State the preparation type.
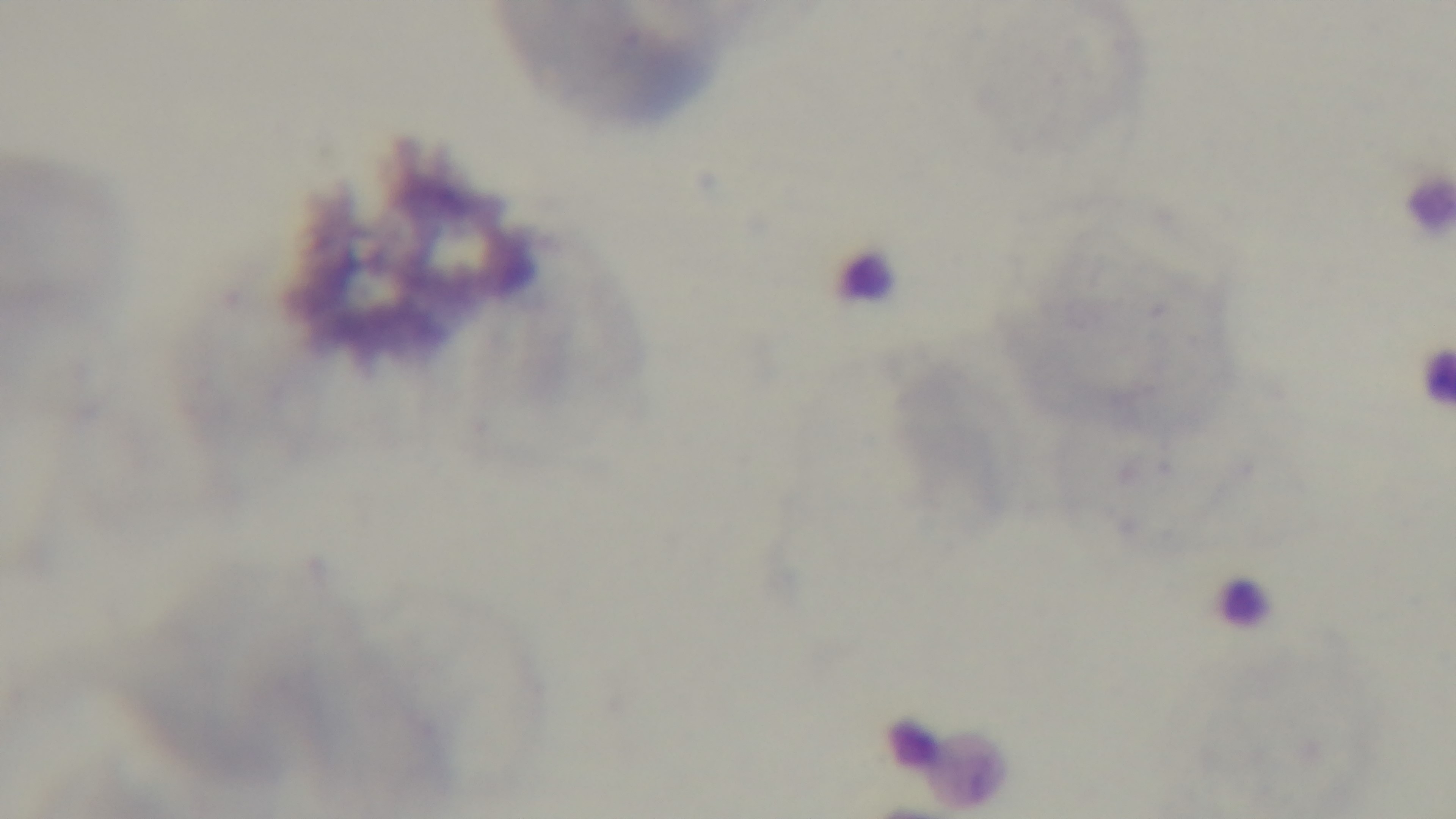

It is a thin blood film.

Summary:
  - Field of view: single
  - Capture: mounted 4K digital camera
  - Malaria status: negative
  - Objective: 100x oil immersion
  - Stain: Giemsa
  - Modality: light microscopy